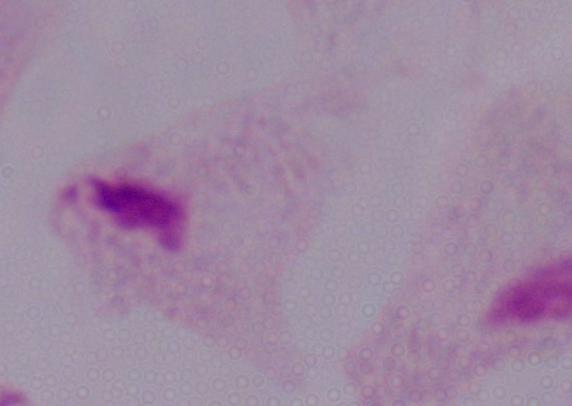

{
  "identification": "trichomonad",
  "magnification": "1000x",
  "modality": "photomicrograph"
}